Find the cells and give the type of each one.
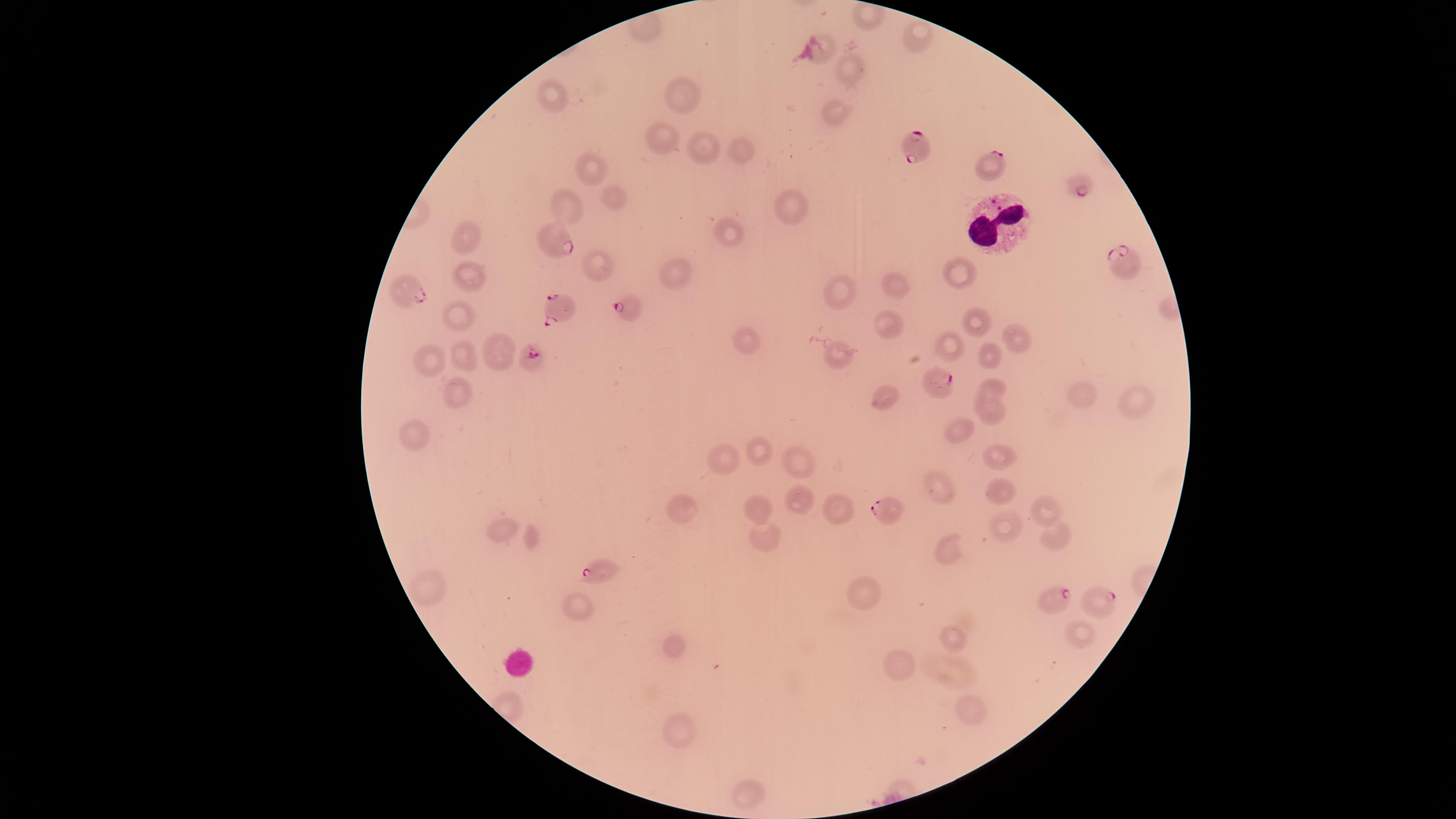
Approximate marker points as [x, y] in pixels.
Parasitized red blood cells: [909, 146], [989, 168], [1078, 184], [559, 244], [1127, 262], [411, 289], [562, 308], [624, 311], [528, 358], [942, 384], [891, 510], [598, 567], [1054, 601], [1096, 601].
Uninfected red blood cells: [916, 37], [847, 71], [683, 89], [555, 93], [831, 115], [664, 136], [708, 146], [746, 150], [593, 169], [615, 201], [566, 203], [791, 211], [726, 232], [472, 237], [595, 266], [958, 271], [673, 272], [468, 275], [896, 282], [842, 288], [460, 313], [887, 321], [974, 321], [1009, 335], [950, 341], [744, 342], [839, 350], [494, 351], [466, 352], [989, 353], [431, 361], [993, 386], [1080, 390], [456, 392], [888, 397], [1136, 402], [989, 410], [959, 426], [420, 427], [762, 454], [996, 456], [792, 457], [724, 461], [941, 486], [994, 490], [797, 500], [762, 506], [837, 506], [1043, 508], [687, 513], [1006, 529], [505, 532], [1053, 533], [761, 538], [532, 541], [951, 546], [424, 587], [862, 592], [572, 607], [1085, 631], [959, 634], [676, 643], [901, 663], [970, 704], [681, 727], [748, 790].
White blood cells: [999, 223].

{
  "visible_region": "circular",
  "stain": "Giemsa",
  "species": "Plasmodium falciparum",
  "field_of_view": "single",
  "capture": "smartphone photograph through the microscope eyepiece",
  "image_size": "1456×819 pixels",
  "preparation": "thin blood smear"
}